State the blood parasite species.
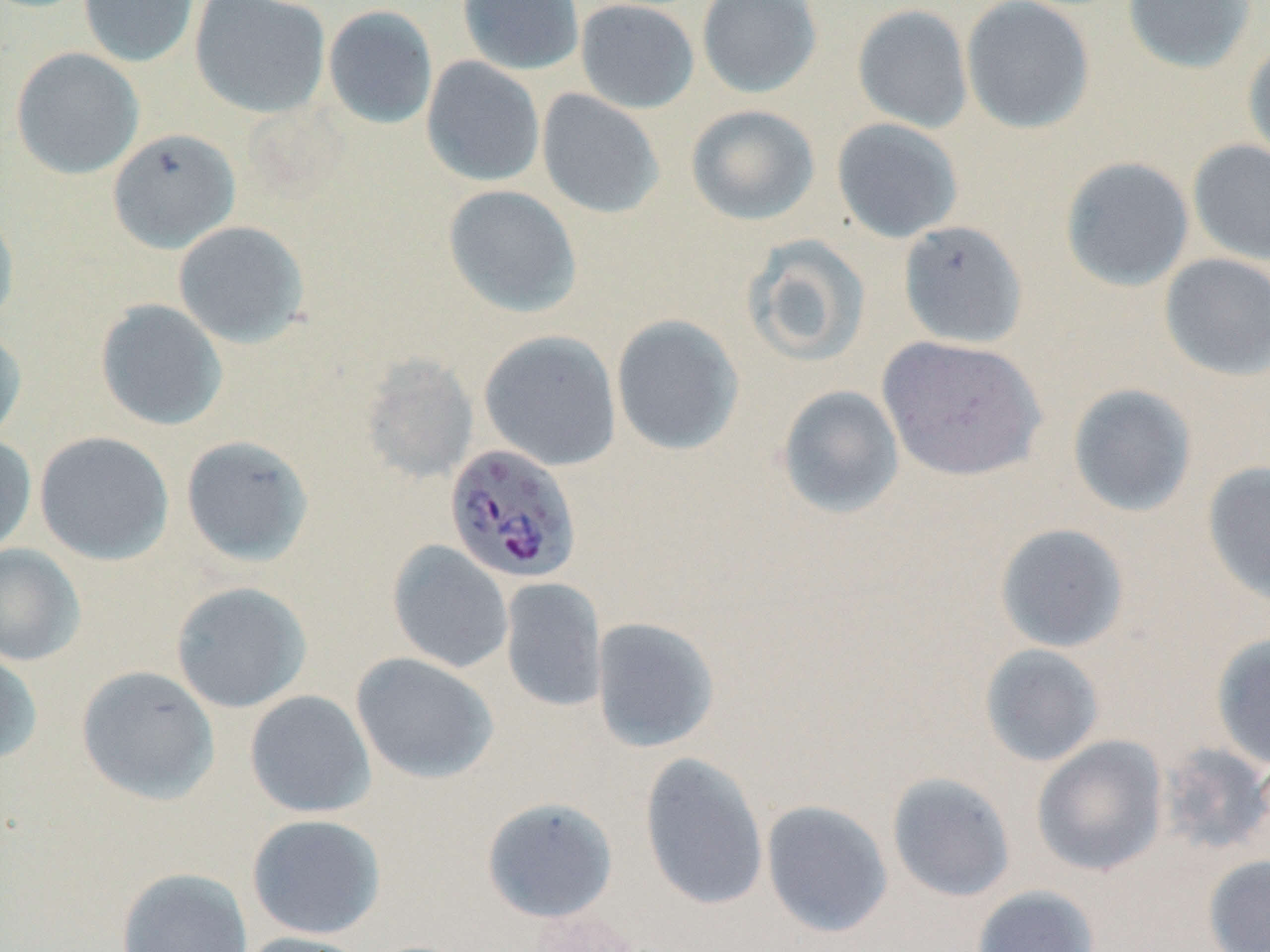

Plasmodium falciparum.

Summary:
  - Coordinate format: approximate bounding boxes as (x1, y1, x2, y2) in pixels
  - Uninfected red blood cell locations: (78, 0, 200, 68), (189, 0, 331, 119), (457, 0, 584, 75), (575, 0, 700, 114), (696, 0, 823, 98), (960, 0, 1096, 135), (1121, 0, 1257, 74), (852, 4, 974, 134), (323, 5, 438, 129), (1242, 38, 1270, 169), (10, 47, 144, 180), (421, 56, 545, 188), (536, 89, 665, 219), (685, 104, 820, 226), (831, 118, 964, 243), (108, 128, 241, 253), (1188, 139, 1270, 265), (1060, 156, 1195, 292), (442, 184, 582, 318), (0, 209, 20, 328), (173, 220, 309, 348), (898, 220, 1029, 349), (743, 235, 872, 367), (1158, 253, 1270, 381), (95, 299, 228, 431), (611, 314, 745, 456), (0, 326, 27, 446), (478, 329, 622, 471), (877, 335, 1047, 482), (359, 353, 479, 483), (1066, 383, 1198, 518), (777, 384, 905, 519), (34, 431, 174, 565), (0, 434, 37, 557), (180, 435, 315, 567), (1202, 461, 1270, 606), (994, 523, 1130, 653), (387, 540, 513, 673), (0, 543, 86, 667), (500, 577, 607, 712), (170, 581, 312, 713), (591, 617, 720, 753), (1210, 632, 1270, 771), (979, 644, 1105, 767), (0, 647, 43, 766), (350, 652, 499, 785), (75, 665, 220, 805), (244, 690, 377, 818), (1031, 735, 1168, 876), (1157, 743, 1270, 858), (638, 752, 770, 911), (886, 771, 1016, 903), (481, 796, 618, 923), (760, 799, 894, 938), (246, 814, 386, 940), (1203, 854, 1270, 952), (116, 867, 253, 952), (972, 885, 1100, 952), (528, 906, 643, 952), (236, 932, 376, 952)
  - Plasmodium falciparum-infected red blood cell locations: (444, 443, 582, 585)
  - Preparation: thin blood film
  - Field of view: one of a larger specimen
  - Magnification: 1000x
  - Modality: light microscopy
  - Image size: 1270×952 pixels
  - Stain: May-Grünwald-Giemsa